Name the blood parasite species.
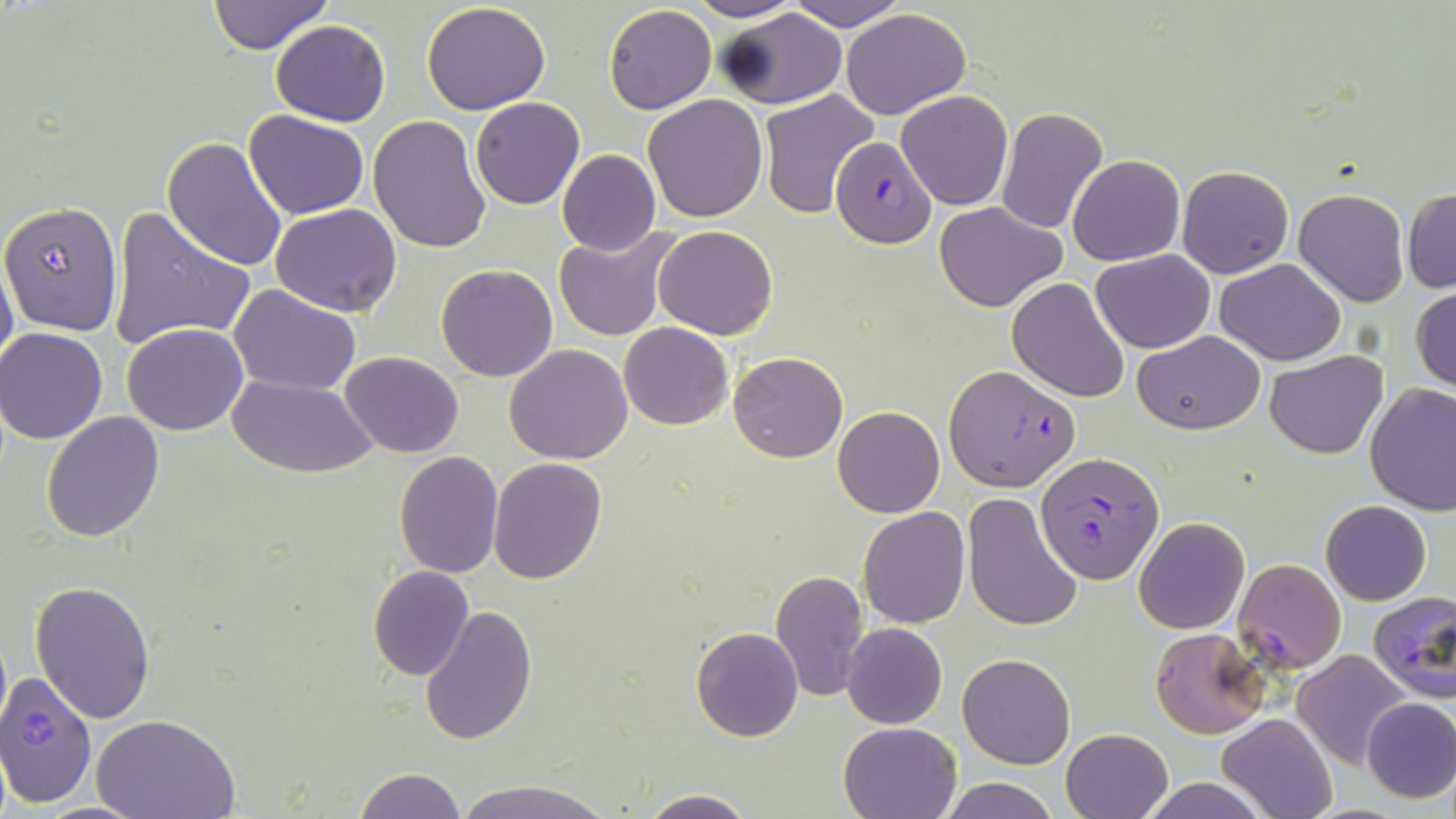

Plasmodium falciparum.

image size = 1456×819 pixels
Plasmodium falciparum-infected red blood cell locations = approximate bounding boxes as (x1,y1)-(x2,y2) corner pairs in pixels: (829,138)-(936,248), (945,363)-(1078,491), (1036,453)-(1165,582), (1232,558)-(1345,673), (1367,592)-(1456,703), (1148,625)-(1271,737), (0,676)-(98,806)
uninfected red blood cell locations = approximate bounding boxes as (x1,y1)-(x2,y2) corner pairs in pixels: (205,0)-(334,53), (682,0)-(806,22), (784,0)-(910,31), (422,2)-(551,114), (604,5)-(716,114), (840,8)-(971,118), (717,9)-(848,111), (270,19)-(391,126), (758,90)-(880,218), (897,91)-(1013,210), (642,94)-(768,223), (470,98)-(585,209), (995,105)-(1107,235), (243,109)-(368,219), (369,115)-(490,253), (164,136)-(289,271), (557,149)-(660,255), (1068,155)-(1184,266), (1176,166)-(1293,279), (1403,187)-(1456,294), (1293,188)-(1409,308), (0,201)-(124,335), (936,202)-(1066,312), (107,203)-(256,353), (271,203)-(402,315), (554,225)-(681,343), (652,225)-(777,340), (1092,250)-(1214,353), (0,251)-(18,380), (1215,259)-(1346,366), (436,264)-(558,382), (1006,278)-(1131,403), (229,284)-(361,396), (1410,288)-(1456,393), (123,322)-(248,435), (618,322)-(734,430), (1,328)-(111,443), (1134,331)-(1264,435), (504,343)-(634,464), (1265,349)-(1386,459), (339,351)-(465,457), (728,351)-(847,463), (227,375)-(376,476), (1365,384)-(1456,518), (832,406)-(944,518), (41,410)-(165,541), (393,450)-(503,577), (487,458)-(606,584), (963,492)-(1083,632), (1321,499)-(1432,604), (858,506)-(970,629), (1135,516)-(1250,634), (367,566)-(475,681), (770,570)-(873,704), (31,581)-(158,724), (419,603)-(537,746), (841,623)-(947,729), (691,626)-(804,742), (1293,650)-(1413,769), (957,653)-(1076,769), (1360,697)-(1456,802), (1216,713)-(1337,819), (94,714)-(238,819), (838,720)-(961,818), (1060,728)-(1172,819), (351,768)-(466,819), (939,777)-(1060,819), (1137,777)-(1271,818), (449,779)-(611,819), (637,791)-(757,819), (35,800)-(148,818)
field of view = one of a larger specimen
magnification = 1000x
modality = optical microscopy
stain = May-Grünwald-Giemsa
preparation = thin blood film